Point out each malaria parasite and each leukocyte.
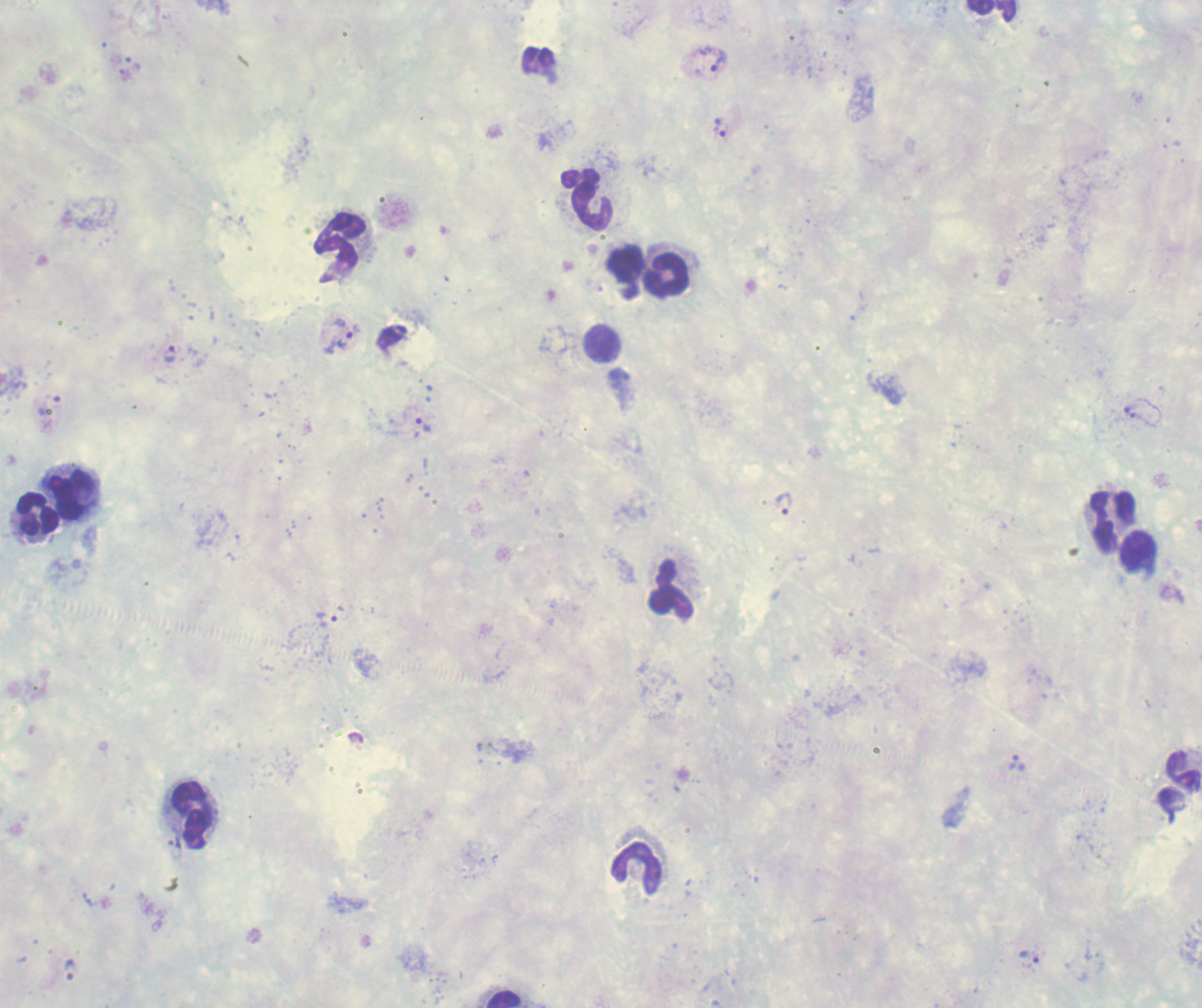
Approximate centers as {x, y} in pixels.
Trophozoites: {135, 62}, {706, 62}, {125, 75}, {721, 129}, {339, 334}, {170, 355}, {48, 408}, {1129, 411}, {418, 421}, {785, 504}, {327, 618}, {1016, 765}, {1030, 957}, {71, 970}.
No schizont or gametocyte forms observed.
Leukocytes: {990, 11}, {538, 60}, {588, 198}, {341, 240}, {622, 269}, {669, 275}, {603, 345}, {71, 495}, {38, 516}, {1108, 520}, {1140, 555}, {670, 591}, {1181, 769}, {192, 817}, {634, 865}, {501, 997}.

field of view = single
preparation = thick smear of blood
magnification = 100x
stain = Romanowsky
image size = 1202×1008 pixels
context = previously used in an actual diagnosis
background quality = poor